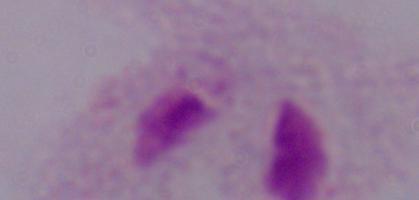

Summary:
  - Magnification: 1000x
  - Modality: photomicrograph
  - Identification: trichomonad